Assess this cell for malaria.
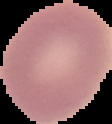

Uninfected.

Image is 112×124 pixels. Segmented cell region on a black background. From a thin blood film.